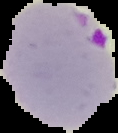
Summary:
  - Image size: 118×133 pixels
  - Image type: segmented cell region with the area outside set to black
  - Preparation: thin blood smear
  - Result: malaria parasites detected